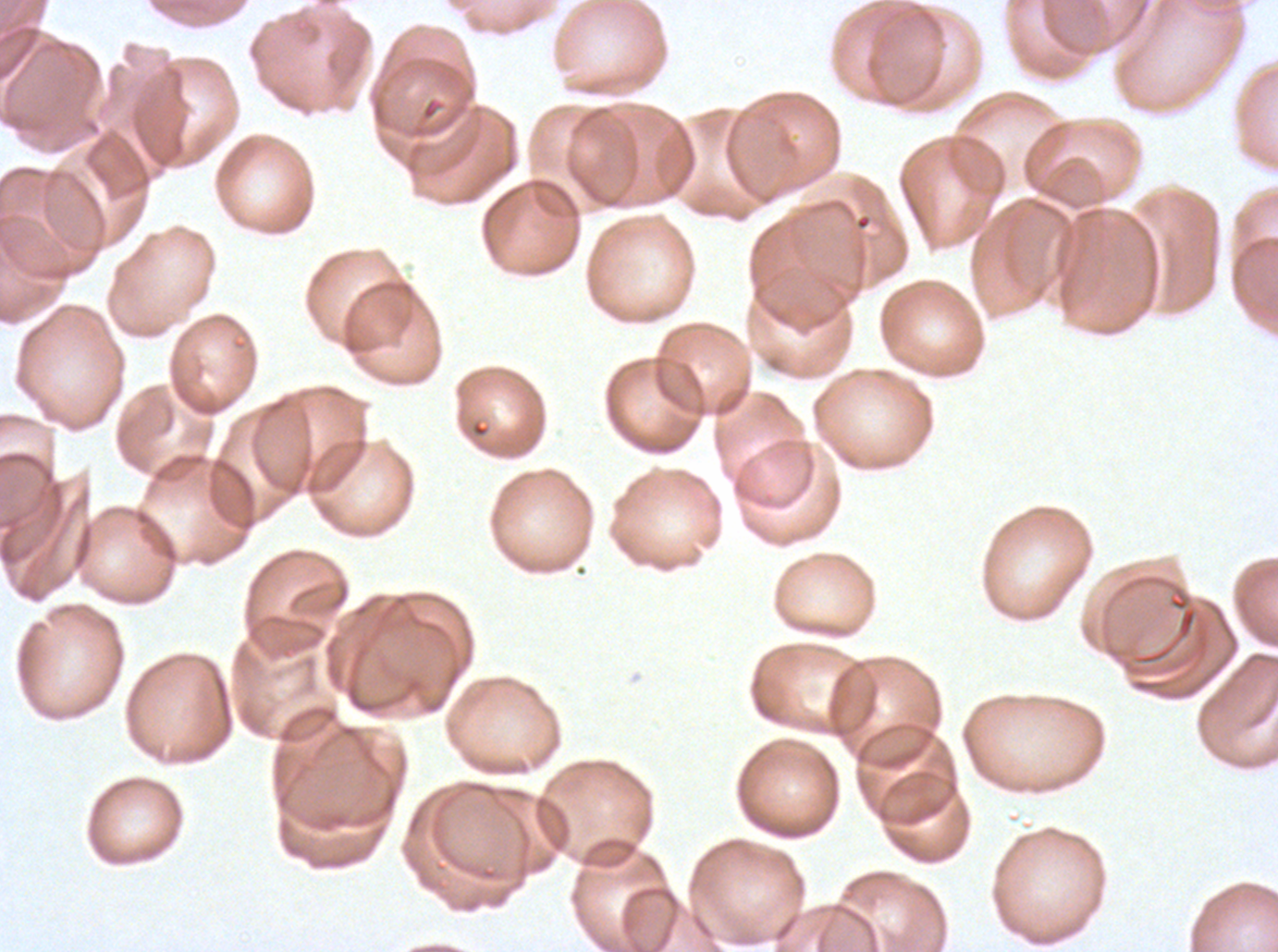
notation = approximate bounding boxes as (x1, y1, x2, y2) in pixels
debris locations = (1132, 585, 1198, 665)
image size = 1278×952 pixels
field of view = sub-image separated from a larger composite
specimen = Plasmodium falciparum cultured ex vivo for 24 to 48 hours, from a patient in The Gambia
preparation = thin blood film
stain = Giemsa